Point out every malaria parasite.
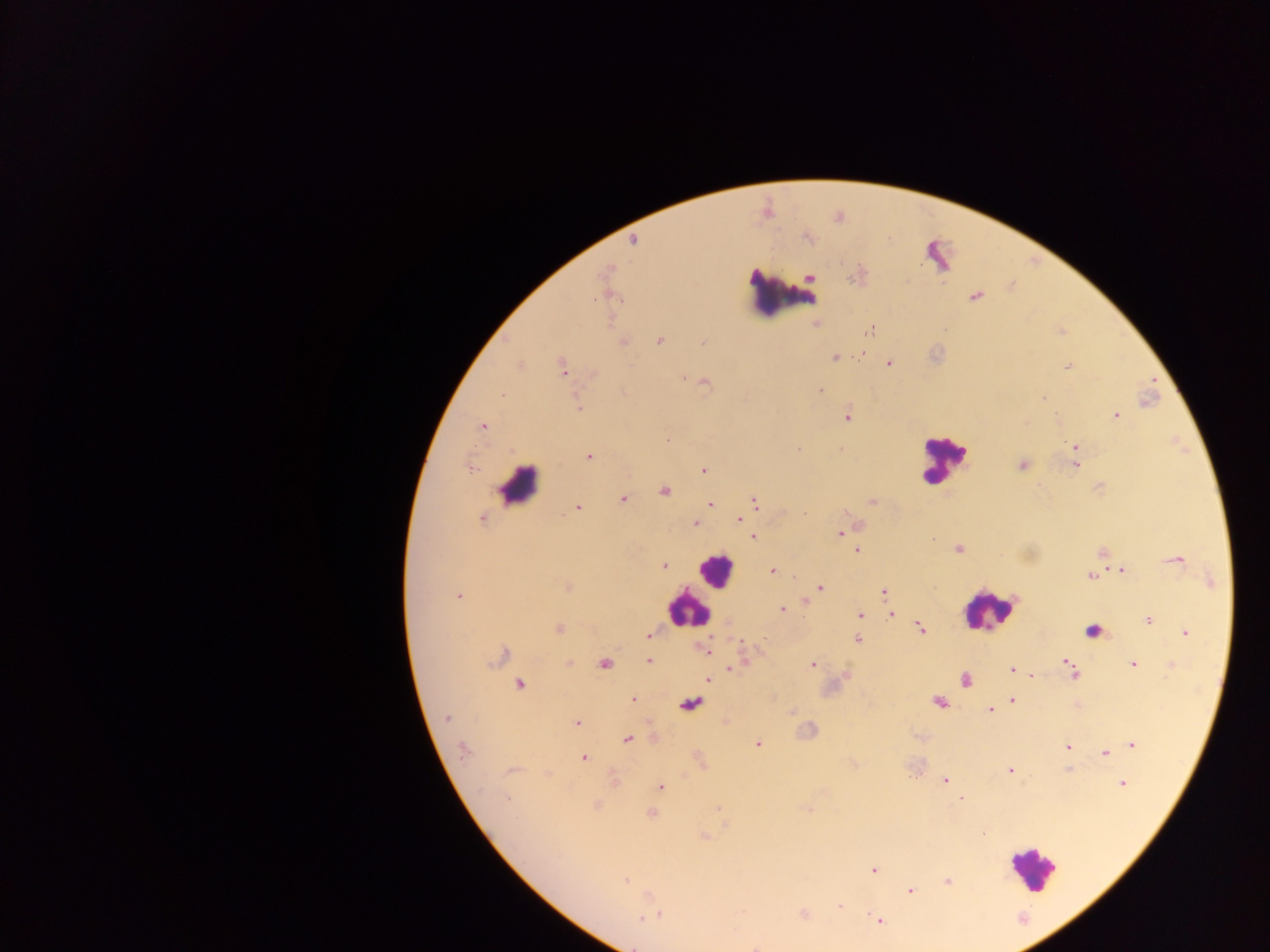

Approximate centers as {x, y} in pixels.
Malaria parasites: {633, 240}, {608, 268}, {808, 277}, {609, 292}, {974, 296}, {816, 324}, {868, 331}, {659, 340}, {623, 341}, {703, 342}, {862, 351}, {834, 358}, {889, 363}, {519, 365}, {1067, 366}, {563, 368}, {684, 376}, {704, 381}, {819, 390}, {502, 394}, {1044, 398}, {579, 408}, {1116, 414}, {848, 415}, {482, 427}, {1075, 447}, {798, 449}, {588, 456}, {1074, 456}, {1022, 465}, {1074, 465}, {470, 467}, {702, 469}, {664, 491}, {622, 498}, {754, 500}, {873, 501}, {710, 503}, {577, 506}, {846, 512}, {745, 513}, {481, 517}, {739, 519}, {695, 523}, {839, 533}, {752, 537}, {856, 549}, {957, 549}, {1102, 551}, {1176, 560}, {663, 565}, {772, 570}, {1121, 570}, {1090, 575}, {1211, 581}, {567, 587}, {820, 588}, {884, 592}, {458, 595}, {806, 601}, {782, 609}, {890, 613}, {859, 615}, {1148, 620}, {559, 628}, {858, 628}, {920, 628}, {1093, 630}, {1185, 631}, {647, 634}, {857, 639}, {708, 644}, {706, 650}, {499, 656}, {743, 657}, {648, 661}, {567, 663}, {604, 663}, {812, 664}, {1133, 664}, {1171, 664}, {729, 668}, {1071, 668}, {1011, 669}, {1030, 675}, {845, 676}, {964, 678}, {707, 679}, {519, 684}, {632, 700}, {1011, 700}, {938, 702}, {689, 703}, {1076, 705}, {989, 709}, {791, 711}, {446, 718}, {725, 721}, {576, 723}, {652, 737}, {626, 739}, {757, 744}, {1132, 744}, {1068, 747}, {463, 749}, {1105, 753}, {583, 757}, {699, 760}, {1068, 769}, {510, 770}, {1009, 771}, {548, 773}, {613, 778}, {945, 780}, {1122, 783}, {660, 787}, {658, 789}, {505, 798}, {961, 798}, {596, 805}, {718, 807}, {651, 813}, {703, 836}, {873, 870}, {625, 881}, {948, 881}, {910, 890}, {839, 906}, {651, 914}, {803, 915}, {645, 917}, {878, 920}, {757, 945}.

Summary:
  - Leukocyte locations: {784, 293}, {944, 461}, {518, 484}, {717, 570}, {689, 609}, {989, 610}, {1031, 869}
  - Image size: 1270×952 pixels
  - Capture: mobile-phone photograph through a microscope
  - Country: Ghana
  - Preparation: thick blood film
  - Field of view: single